Locate every Plasmodium vivax-infected red blood cell.
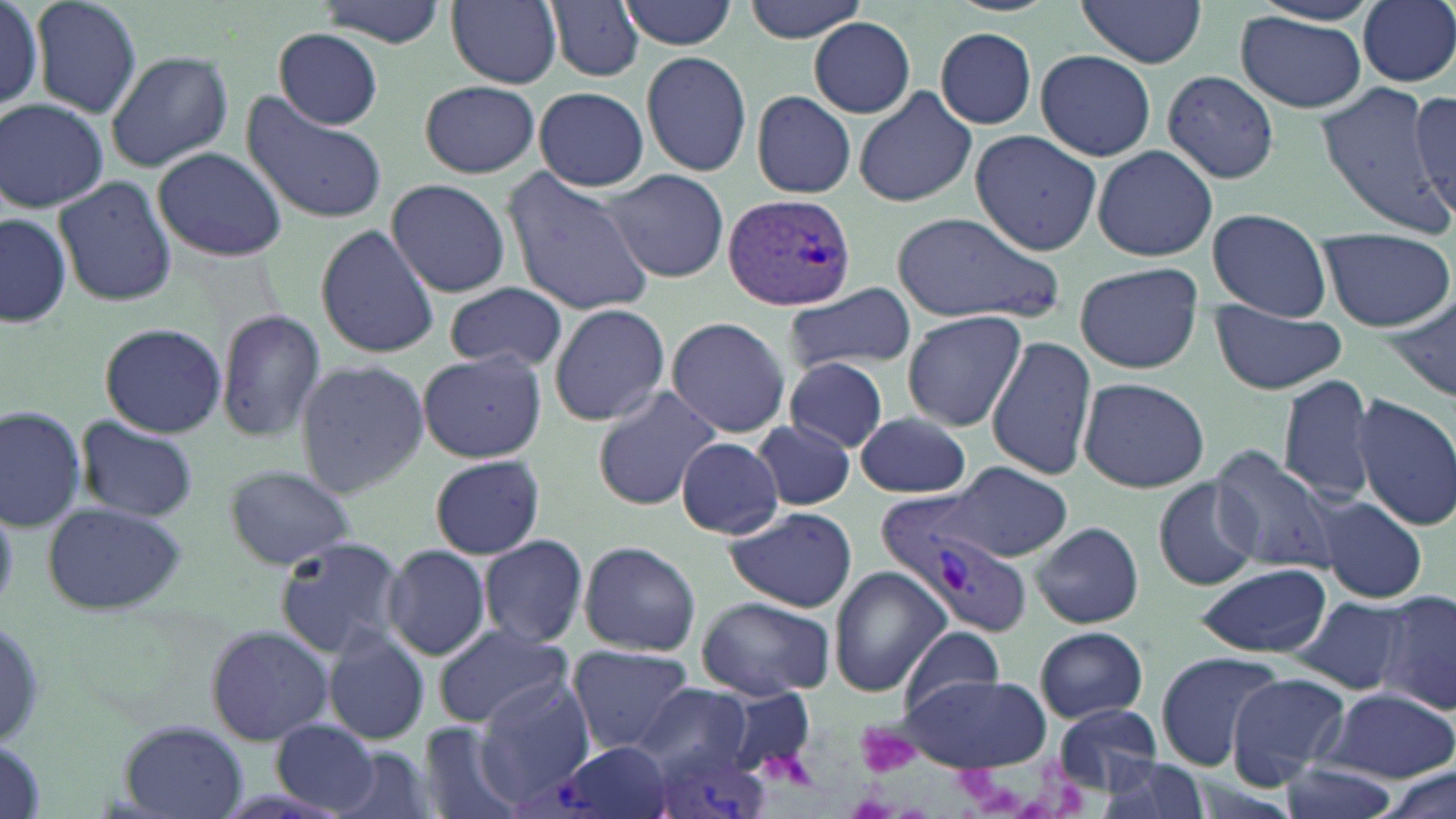
Approximate bounding boxes as named x1/y1/x2/y2 corners in pixels.
Plasmodium vivax-infected red blood cells: (x1=724, y1=193, x2=857, y2=315), (x1=876, y1=500, x2=1035, y2=639), (x1=538, y1=738, x2=676, y2=819), (x1=649, y1=746, x2=772, y2=819).

Uninfected red blood cell locations: (x1=31, y1=0, x2=142, y2=119), (x1=314, y1=0, x2=448, y2=47), (x1=446, y1=0, x2=564, y2=88), (x1=545, y1=0, x2=646, y2=83), (x1=619, y1=0, x2=738, y2=50), (x1=743, y1=0, x2=872, y2=43), (x1=1357, y1=0, x2=1456, y2=87), (x1=0, y1=1, x2=45, y2=110), (x1=1074, y1=1, x2=1209, y2=67), (x1=1236, y1=11, x2=1368, y2=112), (x1=807, y1=18, x2=914, y2=120), (x1=935, y1=27, x2=1039, y2=128), (x1=275, y1=29, x2=384, y2=128), (x1=105, y1=50, x2=233, y2=173), (x1=1035, y1=50, x2=1156, y2=162), (x1=640, y1=51, x2=753, y2=176), (x1=1163, y1=71, x2=1280, y2=184), (x1=419, y1=79, x2=539, y2=178), (x1=1316, y1=79, x2=1447, y2=232), (x1=855, y1=84, x2=980, y2=207), (x1=533, y1=86, x2=649, y2=192), (x1=1407, y1=87, x2=1456, y2=223), (x1=240, y1=90, x2=389, y2=225), (x1=751, y1=90, x2=856, y2=200), (x1=1, y1=100, x2=109, y2=211), (x1=971, y1=131, x2=1101, y2=254), (x1=1093, y1=144, x2=1217, y2=262), (x1=152, y1=146, x2=289, y2=262), (x1=500, y1=168, x2=658, y2=317), (x1=604, y1=169, x2=730, y2=282), (x1=52, y1=175, x2=179, y2=306), (x1=384, y1=178, x2=512, y2=297), (x1=1203, y1=209, x2=1335, y2=322), (x1=891, y1=211, x2=1065, y2=327), (x1=2, y1=213, x2=72, y2=330), (x1=315, y1=224, x2=440, y2=358), (x1=1318, y1=227, x2=1453, y2=332), (x1=1073, y1=261, x2=1203, y2=375), (x1=444, y1=281, x2=569, y2=373), (x1=784, y1=282, x2=916, y2=374), (x1=1383, y1=298, x2=1456, y2=404), (x1=547, y1=303, x2=670, y2=427), (x1=1210, y1=303, x2=1347, y2=396), (x1=902, y1=310, x2=1027, y2=432), (x1=215, y1=311, x2=326, y2=441), (x1=665, y1=315, x2=792, y2=437), (x1=97, y1=321, x2=227, y2=437), (x1=986, y1=335, x2=1097, y2=479), (x1=415, y1=349, x2=547, y2=463), (x1=783, y1=355, x2=890, y2=453), (x1=293, y1=358, x2=430, y2=499), (x1=1277, y1=374, x2=1378, y2=504), (x1=1076, y1=377, x2=1208, y2=493), (x1=591, y1=384, x2=722, y2=511), (x1=1350, y1=393, x2=1456, y2=532), (x1=0, y1=404, x2=88, y2=531), (x1=854, y1=411, x2=973, y2=498), (x1=77, y1=416, x2=200, y2=522), (x1=752, y1=418, x2=854, y2=511), (x1=677, y1=437, x2=785, y2=539), (x1=1208, y1=446, x2=1337, y2=574), (x1=429, y1=454, x2=545, y2=559), (x1=943, y1=462, x2=1072, y2=560), (x1=220, y1=463, x2=357, y2=572), (x1=1152, y1=478, x2=1260, y2=591), (x1=1314, y1=497, x2=1427, y2=603), (x1=41, y1=502, x2=190, y2=616), (x1=724, y1=506, x2=857, y2=612), (x1=1032, y1=522, x2=1143, y2=628), (x1=271, y1=534, x2=407, y2=656), (x1=478, y1=535, x2=588, y2=648), (x1=579, y1=540, x2=701, y2=655), (x1=382, y1=543, x2=492, y2=661), (x1=1194, y1=564, x2=1333, y2=657), (x1=829, y1=567, x2=949, y2=695), (x1=1374, y1=588, x2=1456, y2=715), (x1=1295, y1=594, x2=1414, y2=697), (x1=697, y1=596, x2=836, y2=698), (x1=0, y1=614, x2=52, y2=751), (x1=431, y1=623, x2=572, y2=729), (x1=204, y1=625, x2=333, y2=746), (x1=1035, y1=626, x2=1150, y2=723), (x1=901, y1=627, x2=1006, y2=714), (x1=323, y1=629, x2=432, y2=746), (x1=568, y1=644, x2=696, y2=751), (x1=1153, y1=652, x2=1286, y2=770), (x1=1226, y1=671, x2=1351, y2=786), (x1=899, y1=673, x2=1052, y2=772), (x1=475, y1=676, x2=594, y2=798), (x1=635, y1=682, x2=782, y2=781), (x1=1320, y1=686, x2=1455, y2=782), (x1=1049, y1=706, x2=1165, y2=795), (x1=271, y1=720, x2=380, y2=814), (x1=117, y1=721, x2=250, y2=819), (x1=414, y1=722, x2=530, y2=819), (x1=325, y1=746, x2=437, y2=819), (x1=1092, y1=756, x2=1209, y2=819), (x1=1278, y1=762, x2=1394, y2=819), (x1=1380, y1=767, x2=1454, y2=819). Platelet locations: (x1=856, y1=724, x2=923, y2=781). Slide-level diagnosis: Plasmodium vivax. Image is 1456×819 pixels. 1000x magnification. Light microscopy. Single field of view. May-Grünwald-Giemsa-stained preparation. Thin blood film.